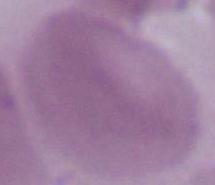
Summary:
  - Modality: micrograph
  - Identification: red blood cell
  - Magnification: 1000x